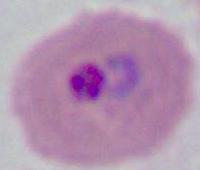 A Plasmodium parasite is seen. Photomicrograph. 400x or 1000x magnification.